Assess the morphology of the erythrocytes.
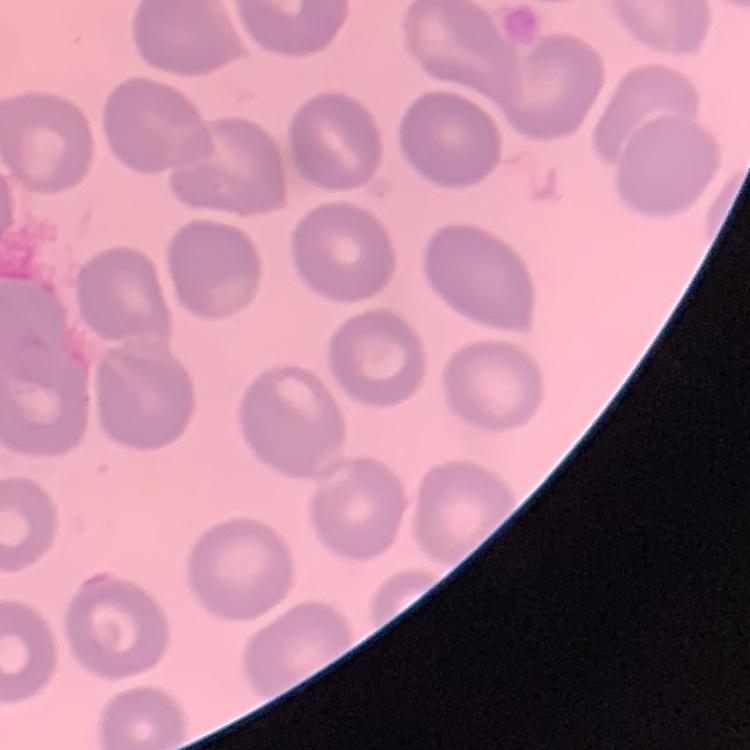
They show no rouleaux formation.

{
  "preparation": "thin peripheral smear",
  "image_type": "one tile cut from a larger photomicrograph",
  "stain": "Field's or Giemsa"
}